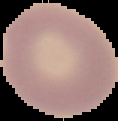
image size = 118×121 pixels
image type = segmented cell region with the area outside set to black
result = no malaria parasites detected
preparation = thin blood smear